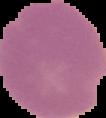
Summary:
  - Image size: 106×118 pixels
  - Result: malaria parasites identified
  - Image type: cell region segmented out of the field of view; surrounding area masked to black
  - Preparation: thin blood film